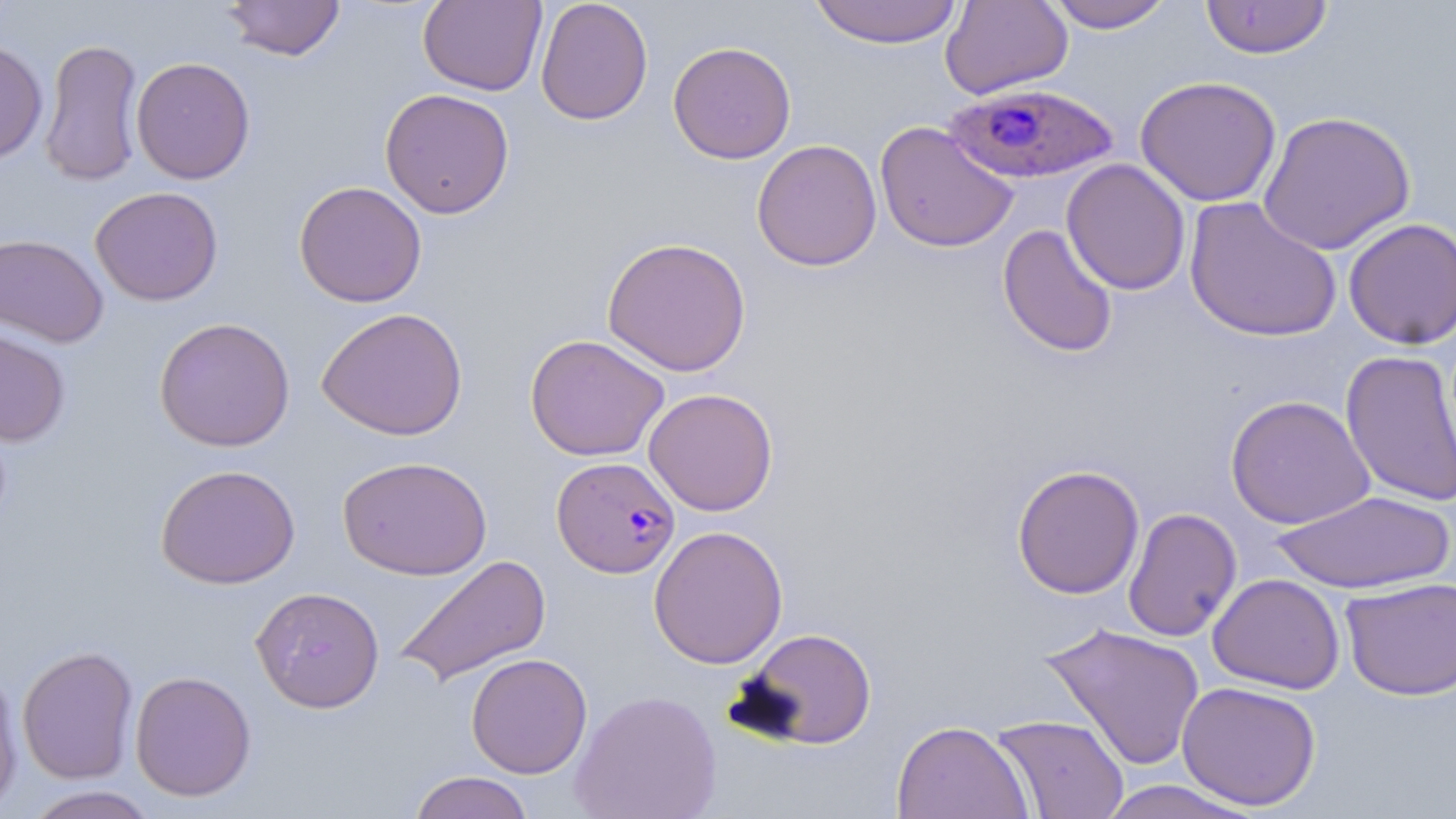
Summary:
  - Coordinate format: approximate bounding boxes as (x1, y1, x2, y2) in pixels
  - Uninfected red blood cell locations: (222, 0, 345, 62), (535, 0, 653, 126), (808, 0, 964, 48), (940, 0, 1073, 99), (1043, 0, 1175, 32), (1200, 0, 1334, 60), (418, 1, 547, 96), (39, 37, 144, 187), (0, 39, 49, 164), (668, 41, 797, 164), (131, 56, 255, 184), (1134, 75, 1282, 206), (379, 88, 515, 219), (1257, 110, 1416, 255), (875, 120, 1019, 253), (751, 139, 882, 272), (1061, 159, 1191, 296), (293, 181, 427, 308), (89, 186, 224, 306), (1184, 196, 1342, 343), (1343, 217, 1456, 350), (997, 223, 1119, 359), (0, 232, 110, 348), (602, 237, 752, 377), (317, 307, 468, 440), (154, 316, 295, 452), (0, 327, 71, 447), (525, 334, 670, 462), (1340, 349, 1456, 509), (643, 387, 779, 516), (1224, 394, 1375, 529), (338, 456, 492, 580), (155, 463, 301, 589), (1011, 464, 1145, 599), (1269, 490, 1455, 594), (1123, 507, 1242, 642), (648, 525, 788, 669), (392, 554, 552, 687), (1207, 573, 1345, 694), (1340, 577, 1456, 701), (252, 586, 385, 712), (1041, 622, 1206, 771), (736, 626, 877, 749), (16, 644, 139, 784), (466, 653, 593, 779), (0, 667, 24, 815), (130, 670, 257, 801), (1176, 680, 1322, 811), (570, 689, 722, 819), (990, 714, 1129, 819), (892, 719, 1033, 819), (408, 771, 535, 819), (1095, 780, 1260, 818), (21, 786, 161, 818)
  - Plasmodium falciparum-infected red blood cell locations: (944, 81, 1120, 184), (551, 457, 681, 577)
  - Slide-level diagnosis: Plasmodium falciparum
  - Field of view: single
  - Image size: 1456×819 pixels
  - Magnification: 1000x
  - Preparation: thin blood film
  - Modality: light microscopy
  - Stain: May-Grünwald-Giemsa